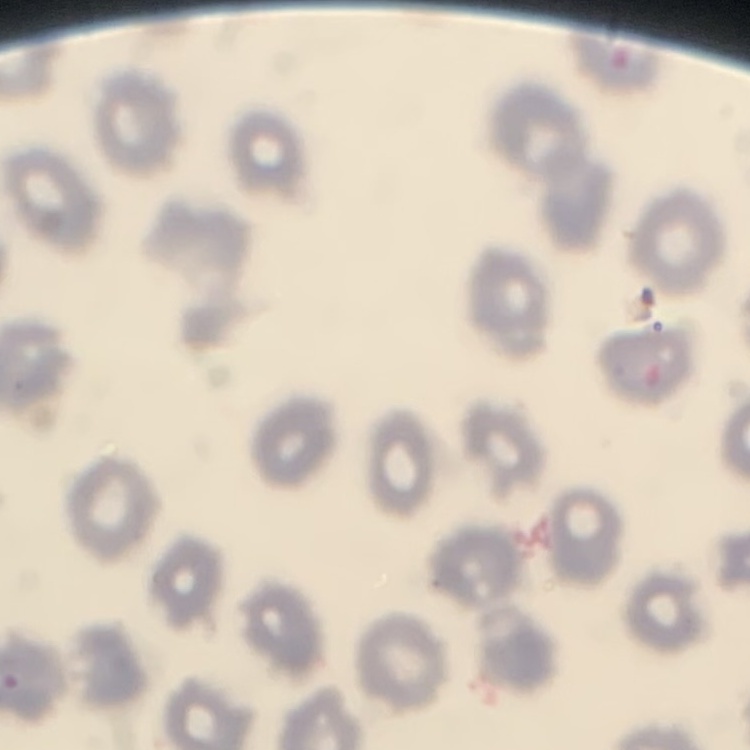
The red blood cells exhibit no rouleaux formation. Square crop of a larger photomicrograph. Thin blood smear. Field's or Giemsa stain.